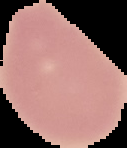
Summary:
  - Image type: cell region segmented out of the field of view; surrounding area masked to black
  - Malaria status: uninfected
  - Image size: 127×148 pixels
  - Preparation: thin blood film